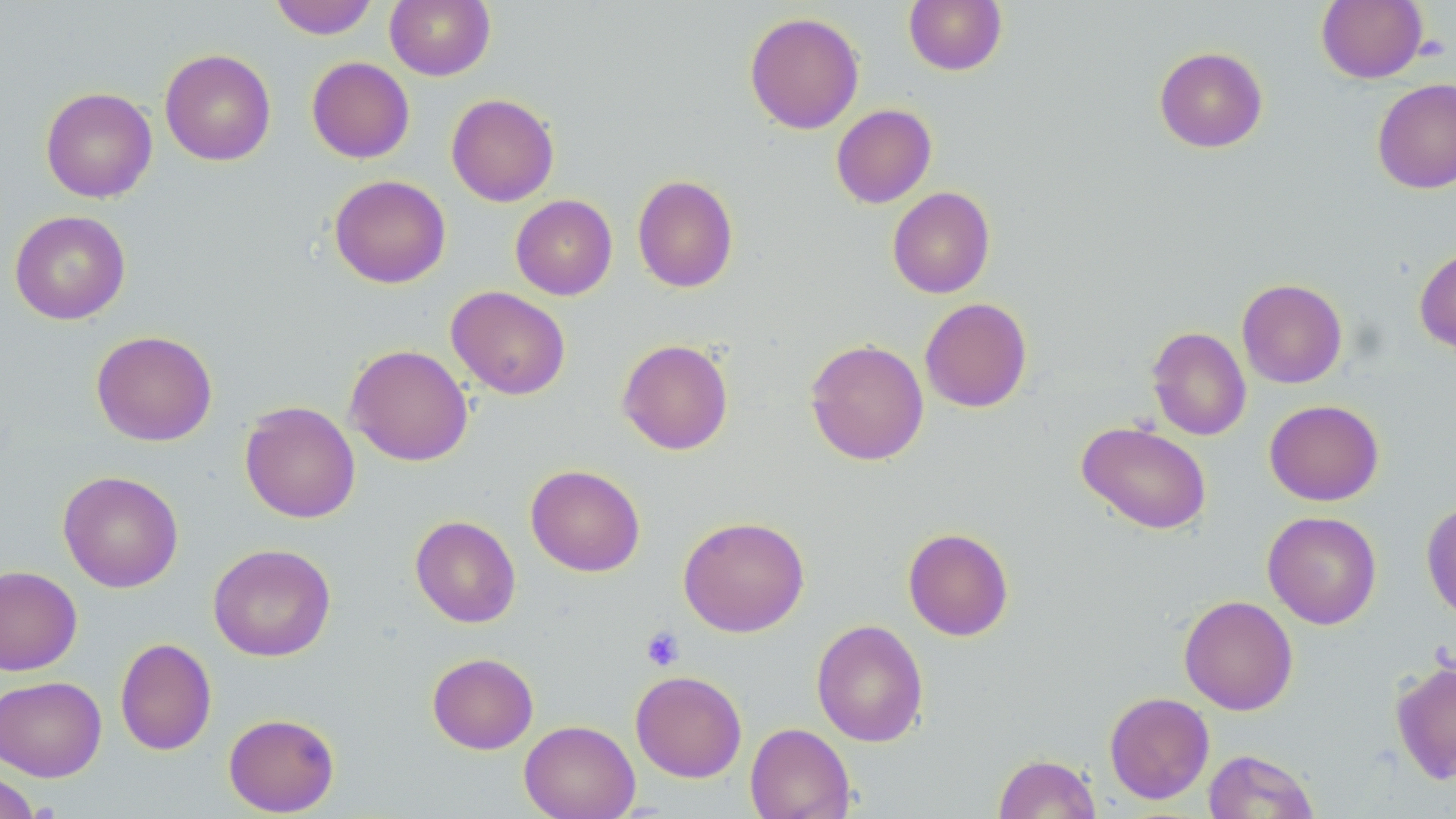

Summary:
  - Coordinate format: approximate bounding boxes as (x1,y1)-(x2,y2) corner pairs in pixels
  - Uninfected red blood cell locations: (268,0)-(380,39), (384,0)-(496,80), (903,0)-(1007,75), (1316,0)-(1428,83), (744,11)-(865,134), (1154,46)-(1268,153), (159,48)-(276,166), (306,57)-(415,163), (1372,78)-(1456,194), (41,86)-(157,203), (446,93)-(559,207), (831,104)-(937,208), (329,174)-(451,288), (632,174)-(738,293), (887,187)-(995,298), (510,194)-(617,300), (9,210)-(130,324), (1414,245)-(1456,355), (1237,278)-(1347,388), (447,286)-(571,400), (920,297)-(1032,413), (1147,326)-(1251,441), (91,330)-(217,446), (805,338)-(929,466), (617,339)-(734,455), (345,344)-(473,467), (1264,399)-(1384,506), (239,401)-(360,524), (1076,421)-(1212,534), (525,464)-(645,577), (58,470)-(184,593), (1421,501)-(1456,621), (1263,511)-(1382,629), (410,515)-(521,628), (678,515)-(810,637), (902,527)-(1014,641), (207,543)-(336,662), (0,565)-(83,676), (1179,594)-(1298,715), (811,619)-(929,747), (115,638)-(217,755), (427,652)-(538,754), (1390,658)-(1456,786), (630,670)-(747,782), (0,676)-(107,781), (1104,692)-(1214,804), (223,712)-(340,816), (519,720)-(639,819), (744,723)-(855,819), (1203,749)-(1319,819), (993,753)-(1102,818), (0,769)-(41,818)
  - Platelet locations: (640,626)-(685,671)
  - Slide-level diagnosis: no evidence of blood parasites
  - Field of view: single
  - Stain: May-Grünwald-Giemsa
  - Preparation: thin blood film
  - Magnification: 1000x
  - Image size: 1456×819 pixels
  - Modality: optical microscopy